State which parasite is depicted.
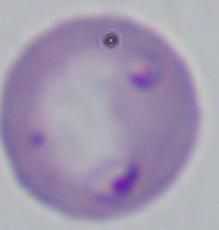

Babesia.

1000x magnification. Photomicrograph.